Locate and identify every blood parasite.
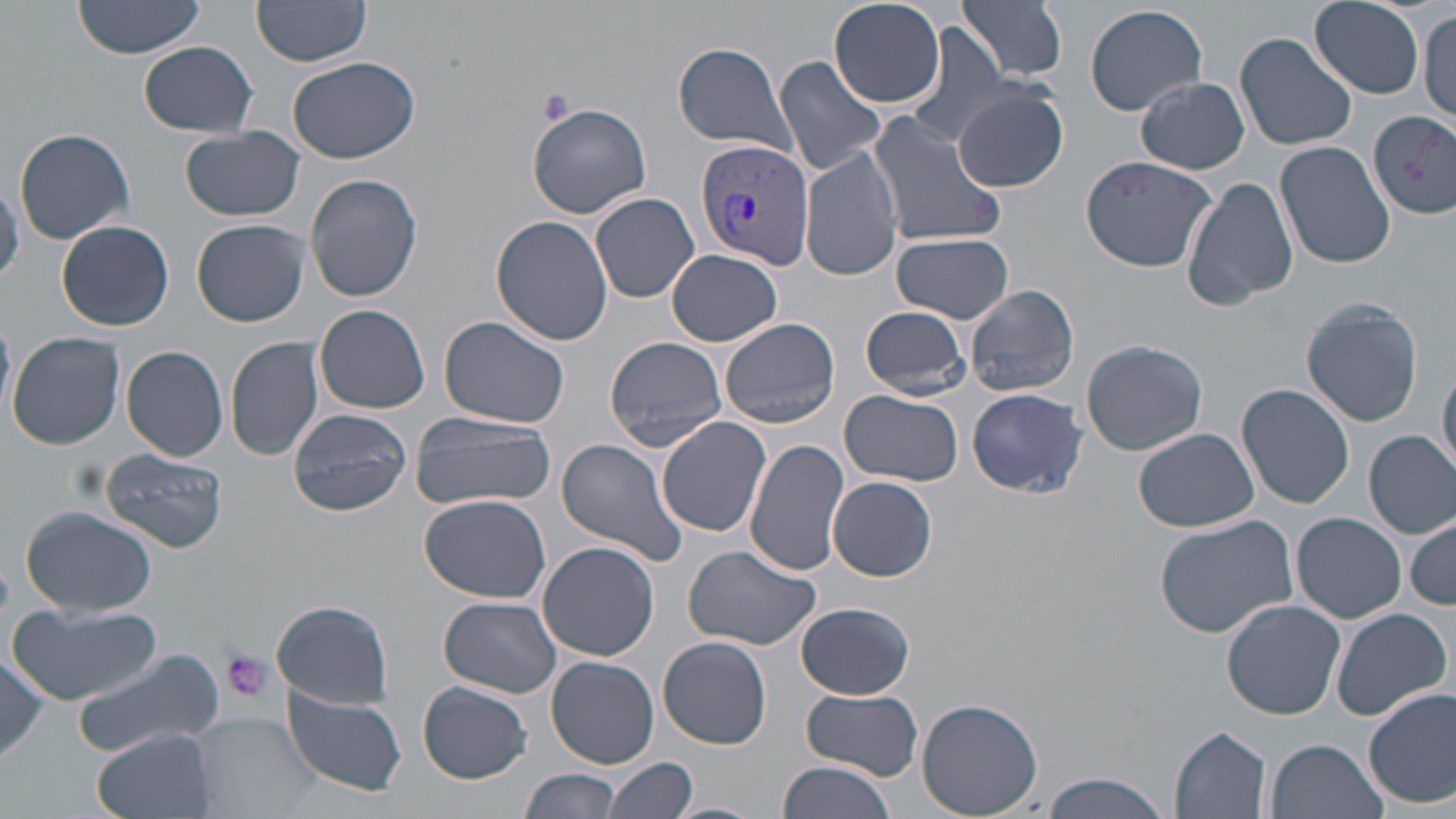
Approximate bounding boxes as (x1,y1)-(x2,y2) corner pairs in pixels.
Plasmodium vivax-infected red blood cells: (695,139)-(813,269).
No Plasmodium falciparum, Plasmodium ovale, Plasmodium malariae, Babesia divergens, or Trypanosoma brucei observed.

Platelet locations: (537,88)-(575,126), (219,647)-(276,703). Uninfected red blood cell locations: (73,0)-(206,59), (959,0)-(1068,82), (253,1)-(371,68), (829,1)-(946,107), (1309,1)-(1426,98), (1085,3)-(1207,116), (1417,9)-(1455,124), (907,23)-(1018,149), (1235,32)-(1358,151), (138,42)-(258,135), (673,42)-(798,155), (289,56)-(418,164), (773,56)-(886,176), (1136,77)-(1249,174), (952,86)-(1068,192), (527,103)-(651,219), (865,108)-(1006,248), (1370,110)-(1456,218), (180,126)-(307,221), (13,128)-(134,244), (1275,140)-(1395,268), (801,143)-(903,282), (1080,154)-(1219,272), (305,172)-(423,302), (1182,174)-(1299,309), (590,192)-(699,303), (491,215)-(616,347), (193,219)-(308,327), (55,220)-(174,331), (890,232)-(1015,324), (667,248)-(782,346), (965,283)-(1079,398), (1299,296)-(1426,428), (317,305)-(431,414), (859,306)-(972,398), (438,316)-(570,428), (719,318)-(841,429), (7,331)-(125,450), (227,336)-(324,462), (605,336)-(731,450), (1081,339)-(1207,457), (120,346)-(228,462), (1438,359)-(1456,479), (1238,383)-(1355,508), (966,388)-(1089,497), (839,391)-(964,487), (289,408)-(411,516), (411,415)-(554,511), (657,415)-(772,538), (1133,427)-(1259,532), (1365,430)-(1456,540), (744,437)-(851,577), (556,439)-(690,568), (101,447)-(226,554), (829,476)-(936,580), (419,494)-(553,601), (18,505)-(157,617), (1292,512)-(1406,624), (1152,514)-(1299,642), (1407,514)-(1456,610), (536,540)-(659,662), (682,543)-(823,648), (440,597)-(563,698), (271,599)-(393,709), (1222,599)-(1346,719), (8,601)-(161,707), (797,602)-(913,699), (1327,607)-(1451,722), (658,635)-(772,749), (74,648)-(227,764), (0,653)-(50,767), (546,655)-(660,769), (418,682)-(531,783), (1362,686)-(1456,810), (802,687)-(923,778), (282,688)-(407,796), (917,698)-(1044,818), (189,712)-(322,819), (1170,726)-(1272,817), (93,727)-(217,819), (1265,738)-(1386,819), (606,758)-(697,817), (777,761)-(898,819), (519,766)-(620,818), (1039,772)-(1172,818), (660,801)-(765,819). Slide-level diagnosis: Plasmodium vivax. Optical microscopy. Image is 1456×819 pixels. Thin blood film. Single field of view. May-Grünwald-Giemsa stain. Captured at 1000x magnification.